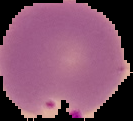
Summary:
  - Image size: 133×121 pixels
  - Preparation: thin blood film
  - Image type: segmented cell region on a black background
  - Malaria status: parasitized